Identify the blood parasite species.
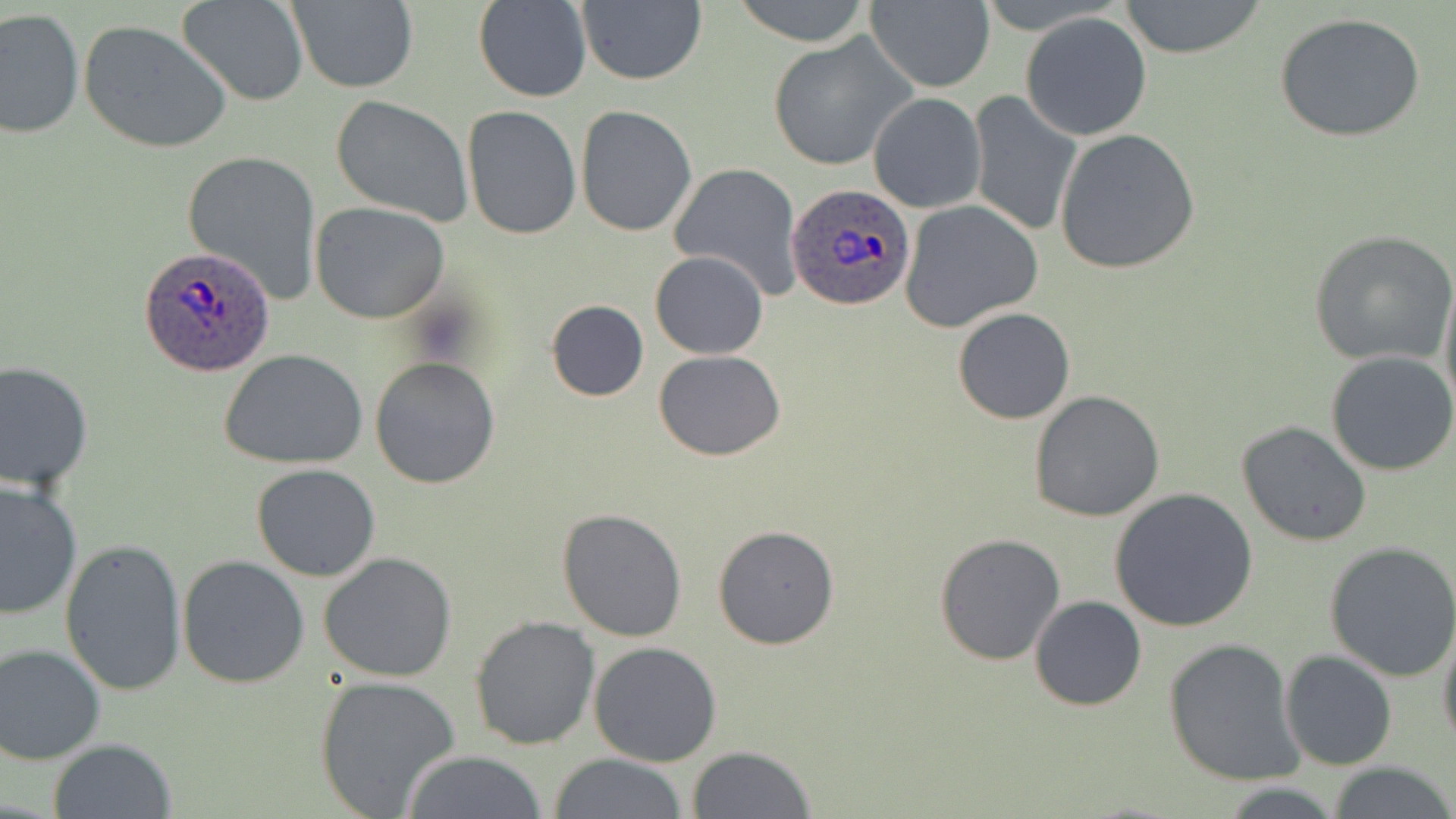

Plasmodium ovale.

image size = 1456×819 pixels
magnification = 1000x
modality = optical microscopy
preparation = thin blood film
uninfected red blood cell locations = approximate bounding boxes as (x1, y1, x2, y2) in pixels: (731, 0, 874, 46), (1116, 0, 1269, 60), (285, 1, 419, 92), (179, 2, 307, 106), (472, 2, 592, 103), (866, 2, 994, 91), (576, 3, 707, 86), (1, 8, 84, 139), (1020, 11, 1153, 141), (1273, 11, 1427, 143), (79, 19, 231, 154), (768, 32, 915, 172), (967, 91, 1082, 238), (868, 93, 985, 213), (328, 95, 476, 228), (461, 106, 581, 240), (576, 106, 697, 237), (1055, 127, 1201, 273), (182, 149, 322, 303), (667, 162, 803, 299), (901, 200, 1043, 332), (310, 201, 451, 323), (1309, 230, 1456, 366), (650, 250, 769, 359), (1438, 267, 1455, 425), (545, 299, 649, 402), (952, 307, 1075, 425), (219, 347, 369, 469), (653, 350, 785, 460), (1326, 351, 1456, 477), (369, 355, 500, 489), (0, 358, 94, 491), (1028, 390, 1167, 523), (1235, 420, 1372, 546), (250, 463, 381, 582), (0, 479, 82, 620), (1108, 487, 1258, 634), (557, 508, 686, 643), (712, 525, 840, 649), (934, 532, 1066, 666), (59, 536, 188, 700), (1325, 541, 1456, 681), (318, 552, 460, 682), (177, 555, 311, 688), (1029, 595, 1146, 711), (469, 617, 601, 752), (1437, 620, 1456, 754), (1163, 637, 1304, 785), (589, 640, 723, 768), (1, 642, 106, 764), (1280, 650, 1397, 769), (314, 675, 462, 818), (47, 738, 179, 819), (686, 746, 816, 819), (400, 750, 548, 819), (548, 754, 689, 819), (1328, 762, 1456, 818), (1218, 783, 1342, 817)
field of view = single
Plasmodium ovale-infected red blood cell locations = approximate bounding boxes as (x1, y1, x2, y2) in pixels: (786, 183, 916, 310), (138, 247, 277, 376)
stain = May-Grünwald-Giemsa